Assess the morphology of the erythrocytes.
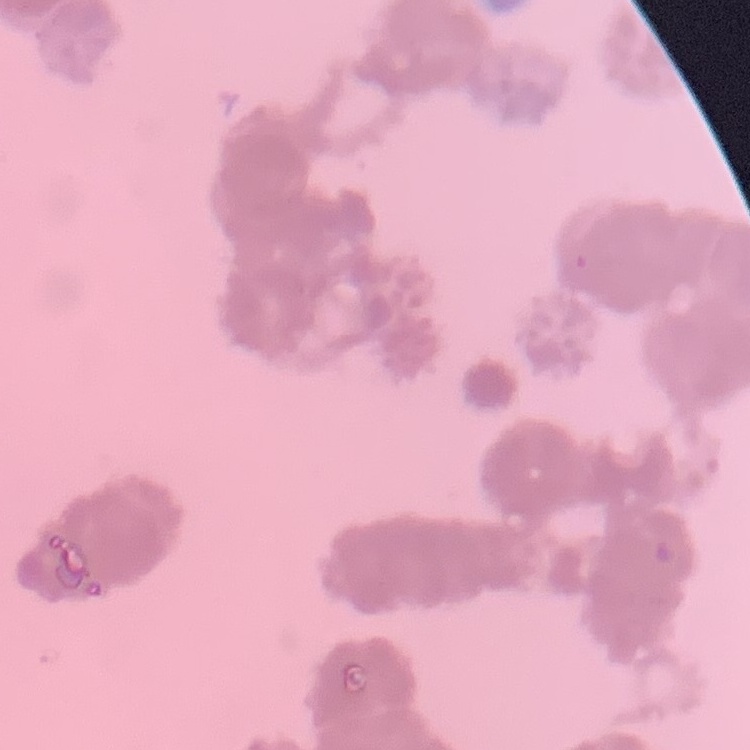

They show rouleaux formation.

stain = Field's or Giemsa
preparation = thin peripheral smear
image type = one tile cut from a larger photomicrograph